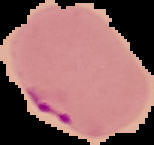
Summary:
  - Malaria status: parasitized
  - Image type: segmented cell region with the area outside set to black
  - Image size: 154×145 pixels
  - Preparation: thin blood film